Locate leukocytes (white blood cells).
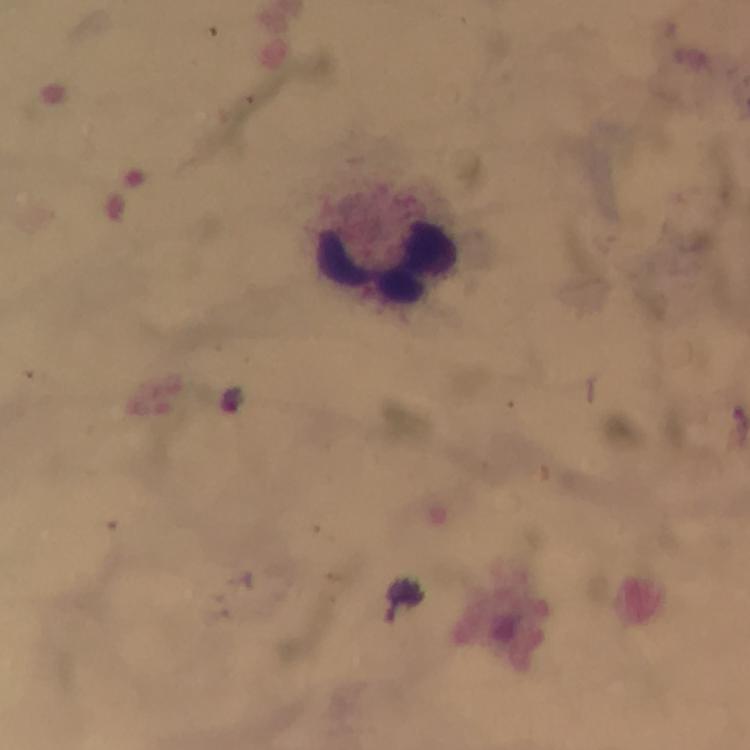
Approximate centers as {x, y} in pixels.
Leukocytes: {387, 261}.

image size = 750×750 pixels
immersion oil = used
context = from a diagnostic examination for malaria
stain = Giemsa
malaria parasite locations = approximate centers as {x, y} in pixels: {229, 399}
cropped from = a single field of view
capture = smartphone mounted on the microscope
preparation = thick blood smear
magnification = 100x